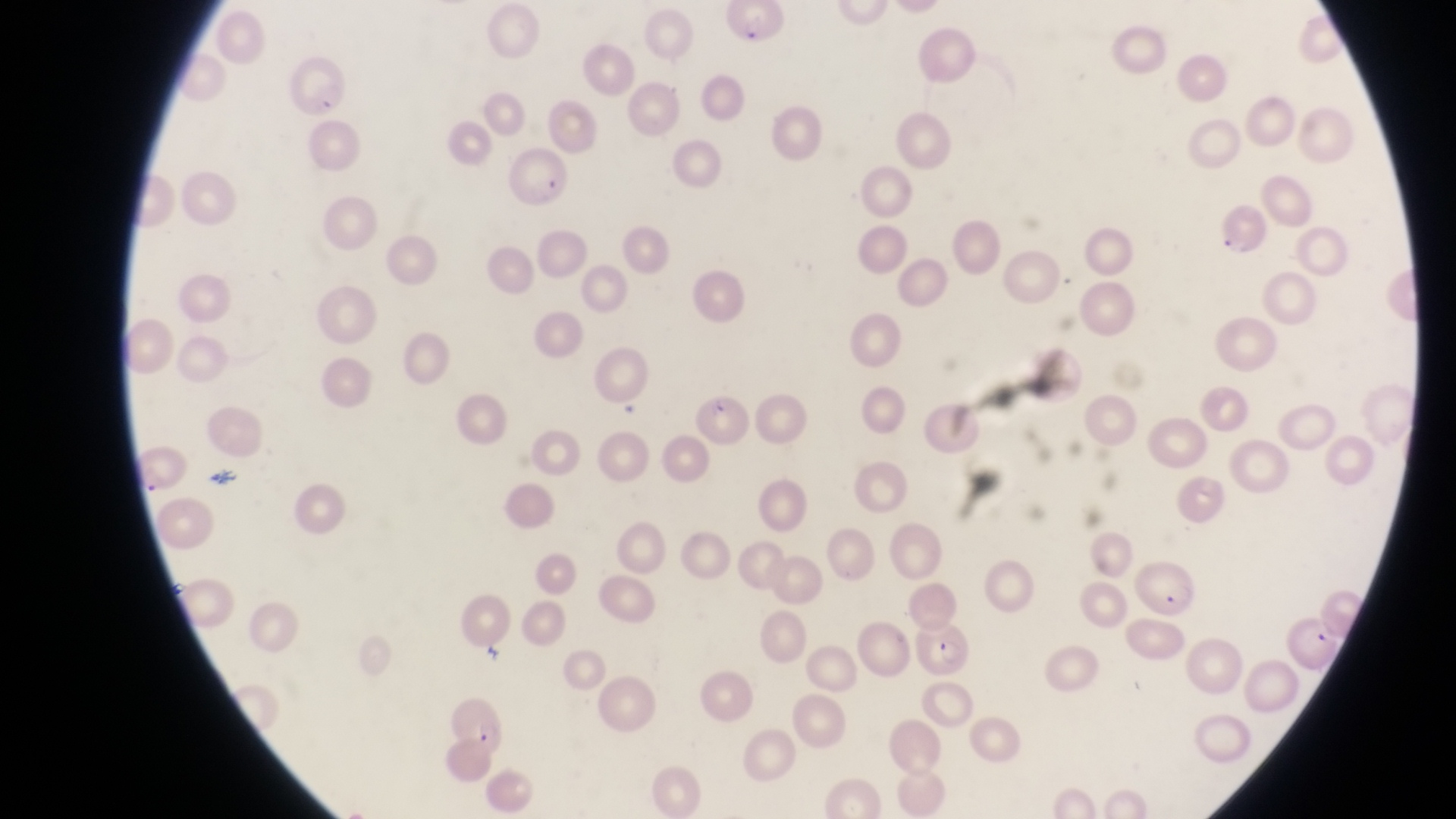
Approximate bounding boxes as {left, top, right, bottom} in pixels.
Summary:
  - Parasitised red blood cell locations: {283, 56, 349, 122}, {507, 145, 573, 209}, {1222, 204, 1274, 260}, {689, 393, 745, 445}, {1134, 563, 1205, 621}, {917, 626, 977, 681}, {446, 703, 506, 755}
  - Preparation: thin blood smear
  - Capture: smartphone photograph through the eyepiece of an Olympus CX-23 microscope
  - Image size: 1456×819 pixels
  - Magnification: 1000x
  - Country: Uganda
  - Field of view: single